Give the extent of all Plasmodium falciparum-infected red blood cells.
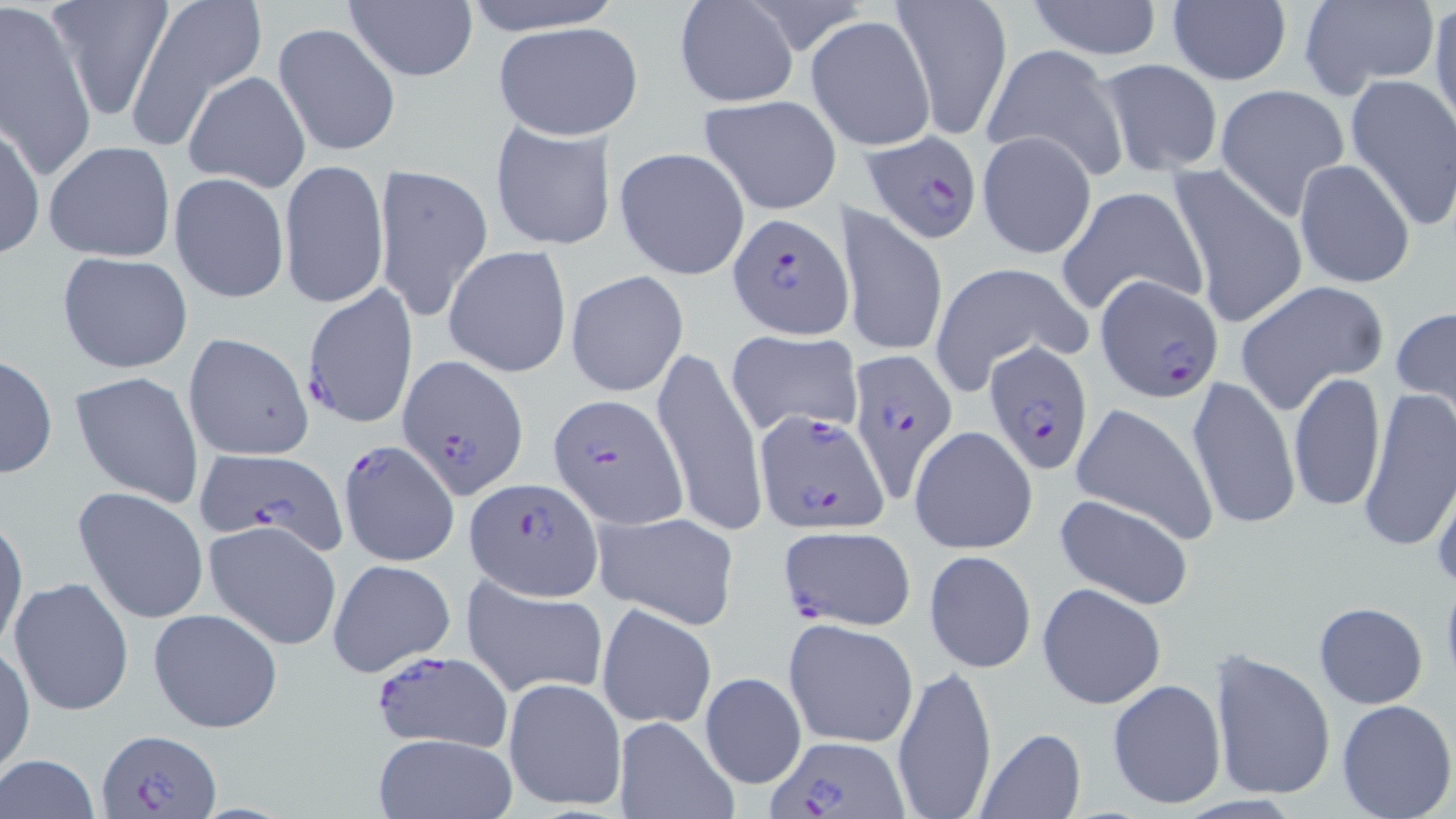
Approximate bounding boxes as named x1/y1/x2/y2 corners in pixels.
Plasmodium falciparum-infected red blood cells: (x1=862, y1=129, x2=986, y2=247), (x1=729, y1=213, x2=852, y2=339), (x1=1096, y1=274, x2=1225, y2=404), (x1=299, y1=284, x2=417, y2=429), (x1=982, y1=341, x2=1093, y2=475), (x1=845, y1=350, x2=957, y2=498), (x1=395, y1=353, x2=527, y2=501), (x1=548, y1=393, x2=687, y2=528), (x1=752, y1=409, x2=889, y2=533), (x1=338, y1=440, x2=462, y2=568), (x1=197, y1=450, x2=353, y2=562), (x1=464, y1=477, x2=601, y2=600), (x1=776, y1=525, x2=914, y2=631), (x1=368, y1=647, x2=515, y2=754), (x1=96, y1=728, x2=221, y2=818), (x1=766, y1=736, x2=907, y2=817).

Summary:
  - Uninfected red blood cell locations: (x1=49, y1=0, x2=173, y2=118), (x1=123, y1=0, x2=266, y2=146), (x1=458, y1=0, x2=624, y2=35), (x1=673, y1=0, x2=799, y2=110), (x1=1026, y1=1, x2=1164, y2=61), (x1=1298, y1=1, x2=1441, y2=99), (x1=1429, y1=1, x2=1456, y2=135), (x1=0, y1=2, x2=97, y2=181), (x1=343, y1=2, x2=478, y2=82), (x1=893, y1=2, x2=1012, y2=138), (x1=1166, y1=2, x2=1291, y2=85), (x1=807, y1=16, x2=937, y2=150), (x1=272, y1=22, x2=400, y2=160), (x1=492, y1=22, x2=642, y2=139), (x1=980, y1=44, x2=1128, y2=181), (x1=1093, y1=58, x2=1226, y2=176), (x1=184, y1=71, x2=311, y2=192), (x1=1344, y1=72, x2=1456, y2=230), (x1=1214, y1=84, x2=1350, y2=218), (x1=698, y1=94, x2=843, y2=214), (x1=489, y1=118, x2=615, y2=253), (x1=0, y1=120, x2=45, y2=261), (x1=977, y1=130, x2=1097, y2=260), (x1=45, y1=140, x2=177, y2=264), (x1=614, y1=147, x2=749, y2=281), (x1=278, y1=158, x2=389, y2=312), (x1=1293, y1=159, x2=1416, y2=288), (x1=375, y1=163, x2=494, y2=321), (x1=1167, y1=163, x2=1310, y2=331), (x1=168, y1=172, x2=290, y2=304), (x1=1056, y1=183, x2=1207, y2=318), (x1=838, y1=204, x2=949, y2=359), (x1=444, y1=245, x2=572, y2=378), (x1=57, y1=251, x2=193, y2=375), (x1=929, y1=261, x2=1090, y2=391), (x1=565, y1=270, x2=688, y2=397), (x1=1233, y1=280, x2=1389, y2=415), (x1=1390, y1=306, x2=1456, y2=414), (x1=725, y1=330, x2=865, y2=435), (x1=182, y1=332, x2=313, y2=461), (x1=653, y1=348, x2=766, y2=535), (x1=0, y1=353, x2=57, y2=480), (x1=69, y1=370, x2=205, y2=507), (x1=1288, y1=372, x2=1385, y2=515), (x1=1186, y1=374, x2=1301, y2=532), (x1=1357, y1=389, x2=1456, y2=557), (x1=1071, y1=403, x2=1219, y2=545), (x1=908, y1=425, x2=1037, y2=556), (x1=1429, y1=467, x2=1456, y2=591), (x1=71, y1=485, x2=211, y2=625), (x1=1052, y1=492, x2=1195, y2=611), (x1=0, y1=510, x2=28, y2=658), (x1=592, y1=511, x2=740, y2=631), (x1=205, y1=520, x2=342, y2=650), (x1=924, y1=550, x2=1036, y2=674), (x1=327, y1=558, x2=456, y2=677), (x1=8, y1=575, x2=136, y2=718), (x1=462, y1=575, x2=608, y2=699), (x1=1037, y1=583, x2=1165, y2=708), (x1=1312, y1=602, x2=1428, y2=709), (x1=596, y1=603, x2=718, y2=728), (x1=149, y1=607, x2=284, y2=735), (x1=782, y1=619, x2=918, y2=749), (x1=0, y1=645, x2=35, y2=776), (x1=1208, y1=649, x2=1336, y2=804), (x1=890, y1=664, x2=998, y2=819), (x1=699, y1=671, x2=807, y2=790), (x1=502, y1=675, x2=627, y2=814), (x1=1107, y1=678, x2=1226, y2=810), (x1=1336, y1=699, x2=1455, y2=818), (x1=612, y1=716, x2=739, y2=819), (x1=976, y1=728, x2=1086, y2=818), (x1=372, y1=732, x2=516, y2=819), (x1=1, y1=755, x2=101, y2=819)
  - Slide-level diagnosis: Plasmodium falciparum
  - Image size: 1456×819 pixels
  - Field of view: single
  - Stain: May-Grünwald-Giemsa
  - Modality: optical microscopy
  - Preparation: thin blood film
  - Magnification: 1000x